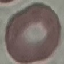
result: no malaria parasites detected
stain: Giemsa
capture: smartphone through the microscope eyepiece
image_type: automatically extracted cell patch, resized to 64 × 64 pixels
preparation: thin smear